Assess this cell for malaria.
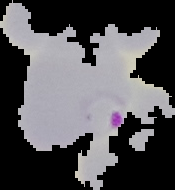
It is parasitized.

Cell region segmented out of the field of view; the surrounding area is masked to black. Image is 175×190 pixels. From a thin blood film.